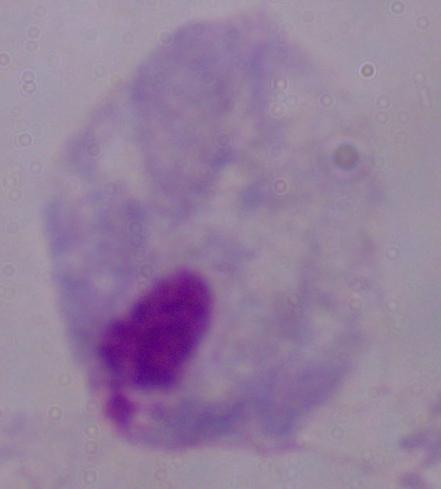 1000x magnification. Photomicrograph. A trichomonad is shown.